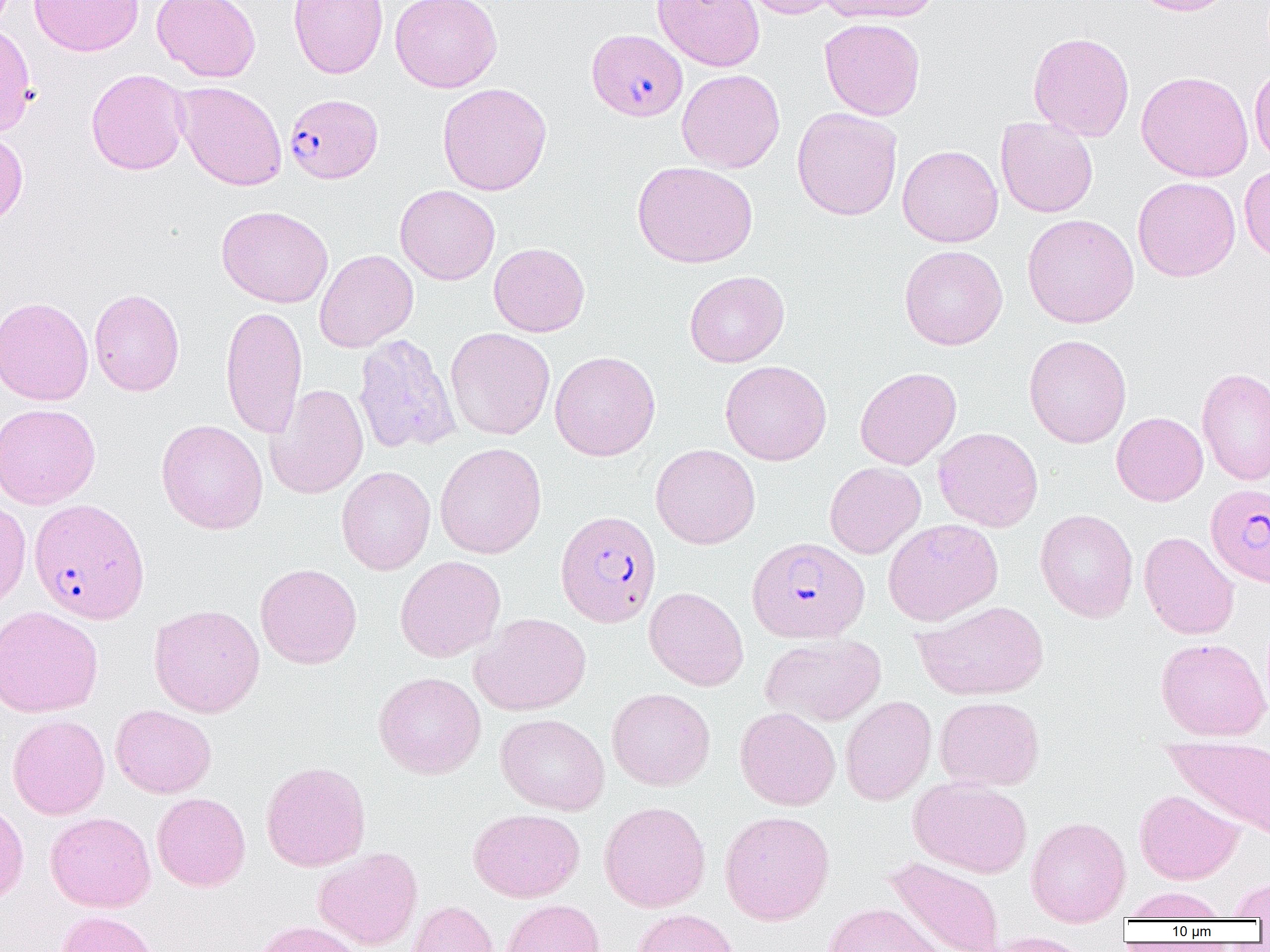
slide-level diagnosis = Plasmodium falciparum
preparation = thin blood film
uninfected red blood cell locations = approximate bounding boxes as named x1/y1/x2/y2 corners in pixels: (x1=29, y1=0, x2=144, y2=56), (x1=151, y1=0, x2=261, y2=82), (x1=160, y1=0, x2=270, y2=164), (x1=288, y1=0, x2=388, y2=79), (x1=389, y1=0, x2=502, y2=93), (x1=652, y1=0, x2=766, y2=71), (x1=739, y1=0, x2=841, y2=19), (x1=817, y1=0, x2=942, y2=23), (x1=1130, y1=0, x2=1236, y2=16), (x1=819, y1=17, x2=925, y2=121), (x1=0, y1=20, x2=36, y2=136), (x1=1028, y1=31, x2=1135, y2=141), (x1=1250, y1=64, x2=1270, y2=167), (x1=86, y1=69, x2=190, y2=175), (x1=677, y1=69, x2=785, y2=173), (x1=1136, y1=70, x2=1253, y2=182), (x1=173, y1=81, x2=287, y2=191), (x1=437, y1=82, x2=552, y2=196), (x1=792, y1=107, x2=903, y2=220), (x1=995, y1=116, x2=1099, y2=218), (x1=0, y1=128, x2=28, y2=227), (x1=897, y1=144, x2=1003, y2=247), (x1=631, y1=161, x2=758, y2=269), (x1=1239, y1=165, x2=1270, y2=263), (x1=1132, y1=177, x2=1240, y2=282), (x1=395, y1=184, x2=500, y2=285), (x1=216, y1=205, x2=333, y2=308), (x1=1022, y1=213, x2=1139, y2=328), (x1=489, y1=242, x2=590, y2=337), (x1=899, y1=245, x2=1008, y2=350), (x1=314, y1=249, x2=418, y2=352), (x1=684, y1=270, x2=789, y2=367), (x1=89, y1=288, x2=184, y2=396), (x1=0, y1=296, x2=94, y2=405), (x1=220, y1=305, x2=307, y2=439), (x1=445, y1=327, x2=555, y2=440), (x1=353, y1=334, x2=461, y2=455), (x1=1024, y1=334, x2=1132, y2=448), (x1=550, y1=350, x2=661, y2=461), (x1=719, y1=360, x2=832, y2=465), (x1=855, y1=367, x2=961, y2=470), (x1=1197, y1=367, x2=1270, y2=486), (x1=265, y1=383, x2=368, y2=499), (x1=0, y1=403, x2=101, y2=509), (x1=1111, y1=412, x2=1208, y2=506), (x1=156, y1=419, x2=268, y2=535), (x1=933, y1=427, x2=1043, y2=532), (x1=435, y1=442, x2=547, y2=559), (x1=651, y1=443, x2=760, y2=549), (x1=824, y1=462, x2=926, y2=559), (x1=336, y1=466, x2=436, y2=575), (x1=0, y1=498, x2=31, y2=611), (x1=1035, y1=509, x2=1138, y2=623), (x1=883, y1=518, x2=1003, y2=626), (x1=1139, y1=531, x2=1239, y2=640), (x1=395, y1=555, x2=506, y2=662), (x1=255, y1=563, x2=362, y2=669), (x1=644, y1=587, x2=749, y2=691), (x1=913, y1=600, x2=1048, y2=700), (x1=148, y1=603, x2=265, y2=718), (x1=0, y1=605, x2=103, y2=717), (x1=470, y1=613, x2=591, y2=716), (x1=761, y1=634, x2=886, y2=726), (x1=1155, y1=637, x2=1270, y2=741), (x1=373, y1=671, x2=486, y2=779), (x1=606, y1=687, x2=716, y2=790), (x1=840, y1=695, x2=936, y2=805), (x1=934, y1=696, x2=1045, y2=791), (x1=110, y1=705, x2=216, y2=798), (x1=734, y1=707, x2=841, y2=810), (x1=496, y1=713, x2=610, y2=815), (x1=7, y1=714, x2=110, y2=820), (x1=1164, y1=737, x2=1270, y2=839), (x1=260, y1=761, x2=371, y2=871), (x1=909, y1=778, x2=1033, y2=878), (x1=1134, y1=789, x2=1244, y2=885), (x1=152, y1=791, x2=251, y2=891), (x1=0, y1=798, x2=29, y2=905), (x1=598, y1=801, x2=711, y2=912), (x1=468, y1=808, x2=584, y2=902), (x1=719, y1=809, x2=835, y2=925), (x1=45, y1=811, x2=156, y2=912), (x1=1026, y1=816, x2=1130, y2=926), (x1=313, y1=847, x2=423, y2=950), (x1=883, y1=856, x2=1005, y2=952), (x1=1225, y1=875, x2=1270, y2=919), (x1=1124, y1=887, x2=1229, y2=921), (x1=501, y1=899, x2=604, y2=952), (x1=406, y1=900, x2=498, y2=952), (x1=824, y1=902, x2=948, y2=952), (x1=632, y1=908, x2=740, y2=952), (x1=54, y1=910, x2=163, y2=952), (x1=252, y1=920, x2=365, y2=952), (x1=982, y1=932, x2=1094, y2=952)
Plasmodium falciparum-infected red blood cell locations = approximate bounding boxes as named x1/y1/x2/y2 corners in pixels: (x1=586, y1=28, x2=687, y2=122), (x1=284, y1=93, x2=383, y2=183), (x1=1206, y1=483, x2=1270, y2=587), (x1=29, y1=498, x2=150, y2=624), (x1=555, y1=509, x2=662, y2=627), (x1=746, y1=536, x2=869, y2=643)
modality = light microscopy
image size = 1270×952 pixels
magnification = 1000x
field of view = one of a larger specimen